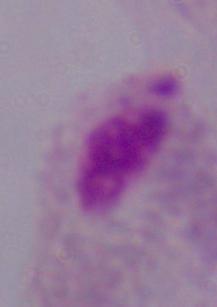

Captured at 1000x magnification. A trichomonad is seen. Photomicrograph.